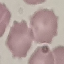
Malaria status: uninfected. Automatically extracted cell patch, resized to 64 × 64 pixels. Giemsa stain. Thin blood smear. Photographed with a smartphone camera at the microscope eyepiece.